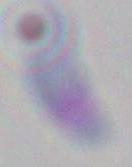

Photomicrograph. Toxoplasma gondii is seen. Captured at 1000x magnification.